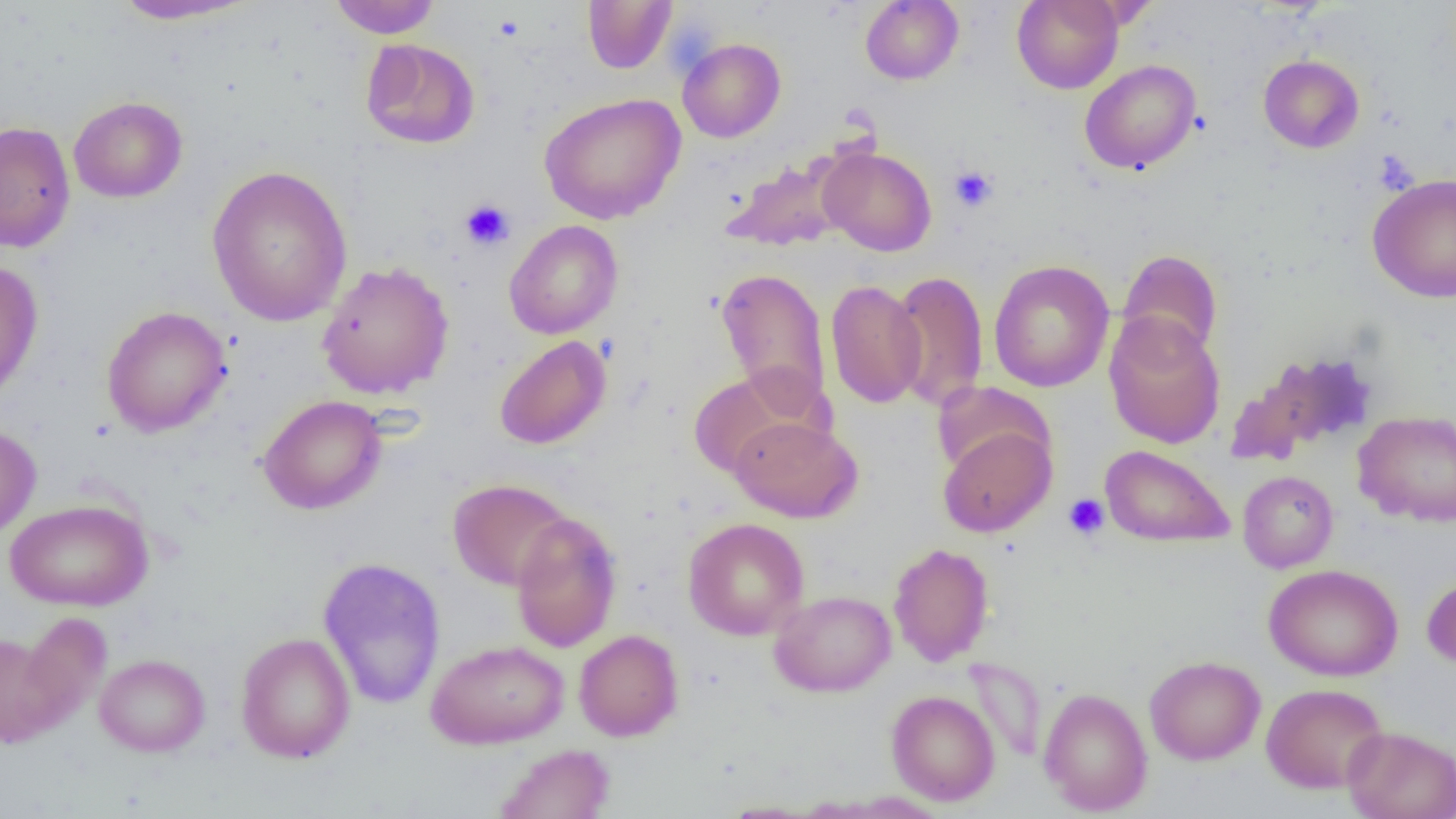
slide_level_diagnosis: no evidence of blood parasites
magnification: 1000x
preparation: thin blood smear
field_of_view: one of a larger specimen
platelet_locations: 'approximate bounding boxes as named x1/y1/x2/y2 corners in pixels: (x1=949, y1=165, x2=998, y2=212), (x1=460, y1=198, x2=515, y2=251), (x1=1063, y1=493, x2=1109, y2=540)'
modality: light microscopy
uninfected_red_blood_cell_locations: 'approximate bounding boxes as named x1/y1/x2/y2 corners in pixels: (x1=110, y1=0, x2=259, y2=25), (x1=328, y1=0, x2=441, y2=38), (x1=860, y1=0, x2=964, y2=85), (x1=1011, y1=0, x2=1124, y2=94), (x1=582, y1=1, x2=677, y2=74), (x1=361, y1=38, x2=480, y2=149), (x1=678, y1=38, x2=786, y2=143), (x1=1258, y1=55, x2=1364, y2=153), (x1=1079, y1=59, x2=1202, y2=174), (x1=539, y1=93, x2=686, y2=224), (x1=68, y1=96, x2=188, y2=203), (x1=0, y1=121, x2=76, y2=252), (x1=819, y1=147, x2=937, y2=256), (x1=722, y1=155, x2=852, y2=252), (x1=206, y1=165, x2=353, y2=326), (x1=1368, y1=173, x2=1456, y2=303), (x1=504, y1=220, x2=623, y2=339), (x1=1117, y1=249, x2=1223, y2=360), (x1=0, y1=259, x2=44, y2=405), (x1=316, y1=260, x2=454, y2=400), (x1=988, y1=260, x2=1115, y2=392), (x1=715, y1=267, x2=832, y2=412), (x1=890, y1=270, x2=989, y2=411), (x1=825, y1=280, x2=927, y2=408), (x1=101, y1=306, x2=232, y2=438), (x1=1104, y1=311, x2=1226, y2=450), (x1=494, y1=335, x2=611, y2=450), (x1=1226, y1=353, x2=1369, y2=466), (x1=687, y1=367, x2=823, y2=479), (x1=933, y1=380, x2=1052, y2=481), (x1=258, y1=395, x2=387, y2=515), (x1=1352, y1=410, x2=1455, y2=526), (x1=729, y1=416, x2=863, y2=523), (x1=0, y1=423, x2=41, y2=541), (x1=937, y1=424, x2=1056, y2=537), (x1=1099, y1=444, x2=1234, y2=548), (x1=1237, y1=470, x2=1338, y2=573), (x1=448, y1=479, x2=573, y2=590), (x1=5, y1=498, x2=154, y2=611), (x1=510, y1=511, x2=622, y2=653), (x1=683, y1=517, x2=809, y2=641), (x1=888, y1=542, x2=995, y2=667), (x1=317, y1=556, x2=447, y2=709), (x1=1264, y1=563, x2=1403, y2=681), (x1=1422, y1=574, x2=1456, y2=669), (x1=769, y1=590, x2=897, y2=697), (x1=14, y1=612, x2=110, y2=734), (x1=573, y1=629, x2=684, y2=741), (x1=0, y1=630, x2=72, y2=749), (x1=235, y1=632, x2=356, y2=763), (x1=426, y1=639, x2=569, y2=749), (x1=94, y1=653, x2=210, y2=757), (x1=1144, y1=655, x2=1266, y2=765), (x1=964, y1=657, x2=1048, y2=763), (x1=1261, y1=683, x2=1389, y2=793), (x1=1038, y1=687, x2=1153, y2=815), (x1=886, y1=690, x2=1000, y2=805), (x1=1343, y1=726, x2=1456, y2=819), (x1=494, y1=743, x2=615, y2=819), (x1=718, y1=801, x2=823, y2=818)'
image_size: 1456×819 pixels